Mark where platelets are.
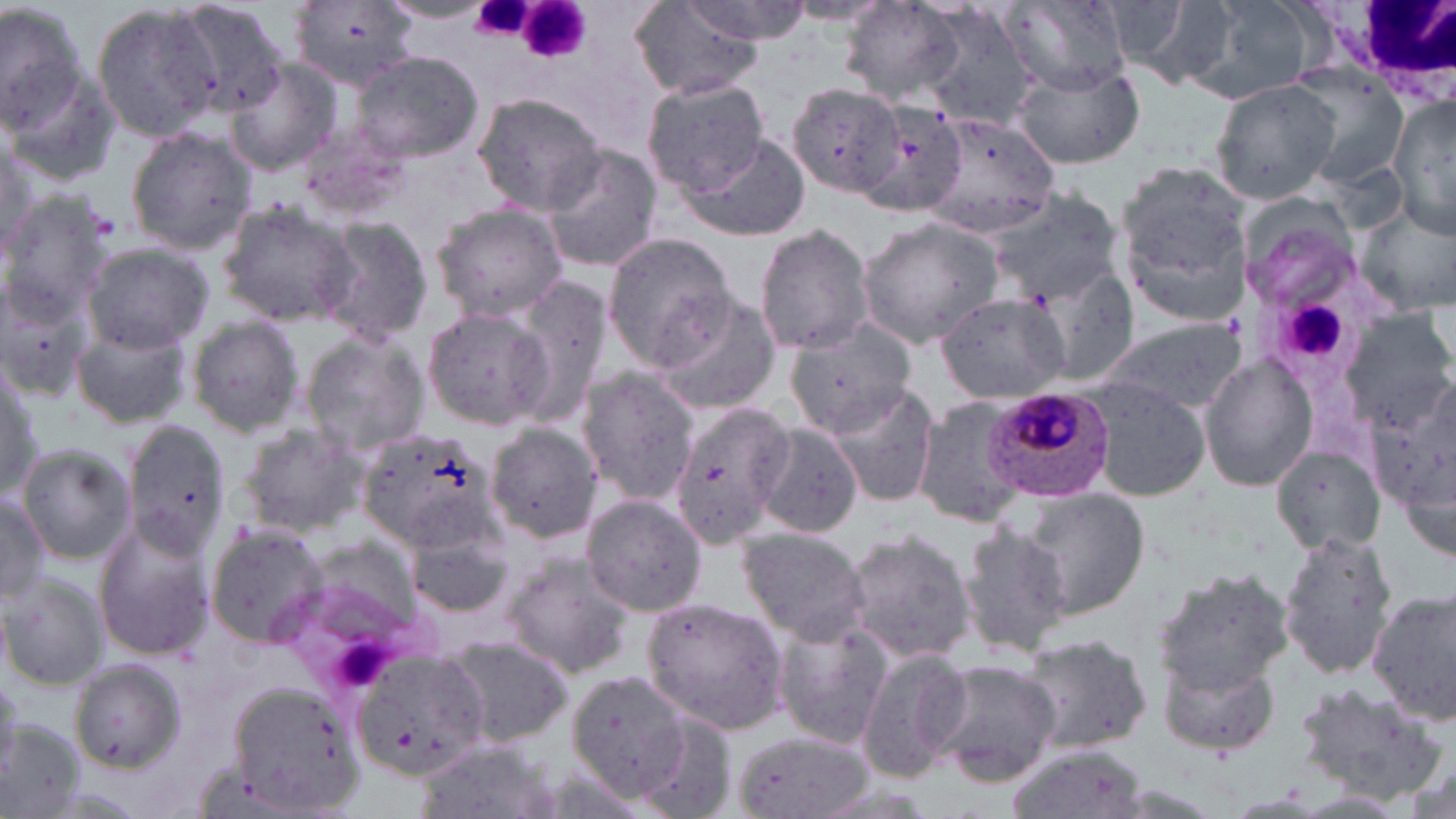
Approximate bounding boxes as (x1, y1, x2, y2) in pixels.
Platelets: (465, 0, 541, 42), (508, 0, 594, 63), (1281, 299, 1343, 360).

Summary:
  - White blood cell locations: (1328, 0, 1456, 98)
  - Uninfected red blood cell locations: (0, 0, 95, 153), (290, 0, 424, 93), (690, 0, 812, 43), (378, 1, 489, 23), (999, 1, 1128, 92), (1117, 1, 1239, 91), (1195, 1, 1322, 106), (788, 2, 890, 26), (839, 2, 968, 104), (168, 4, 297, 111), (629, 5, 764, 98), (906, 5, 1043, 132), (95, 6, 223, 140), (350, 52, 483, 162), (225, 57, 344, 176), (1013, 65, 1143, 169), (1293, 71, 1409, 188), (641, 77, 770, 195), (1210, 79, 1342, 205), (791, 84, 903, 198), (470, 94, 605, 211), (1387, 96, 1455, 238), (863, 102, 970, 215), (922, 113, 1062, 235), (296, 124, 409, 220), (124, 126, 257, 253), (680, 134, 811, 242), (0, 136, 44, 262), (539, 143, 663, 273), (1115, 167, 1253, 322), (983, 188, 1125, 304), (1234, 191, 1360, 310), (0, 192, 114, 322), (1352, 197, 1456, 312), (217, 204, 357, 325), (430, 204, 568, 321), (315, 218, 434, 342), (857, 219, 1003, 349), (754, 224, 877, 355), (604, 233, 737, 365), (81, 242, 214, 352), (1036, 263, 1140, 387), (0, 271, 101, 404), (509, 278, 613, 425), (654, 291, 781, 415), (937, 294, 1070, 404), (1338, 306, 1455, 426), (423, 309, 553, 429), (185, 314, 305, 437), (1098, 317, 1246, 415), (787, 321, 916, 437), (70, 325, 193, 427), (302, 333, 431, 456), (1199, 353, 1318, 492), (1358, 363, 1455, 522), (1, 365, 44, 500), (575, 369, 699, 503), (1085, 379, 1212, 500), (826, 384, 941, 511), (909, 398, 1030, 527), (668, 402, 798, 547), (120, 420, 233, 563), (757, 422, 864, 539), (238, 423, 371, 535), (355, 426, 494, 550), (483, 426, 606, 543), (1273, 443, 1391, 554), (19, 444, 136, 563), (0, 488, 50, 606), (1020, 488, 1149, 619), (581, 495, 706, 616), (92, 517, 219, 662), (957, 521, 1071, 660), (205, 525, 332, 646), (736, 528, 874, 645), (403, 529, 516, 618), (840, 529, 974, 665), (1277, 532, 1396, 681), (315, 542, 419, 632), (502, 554, 637, 678), (1149, 567, 1295, 694), (1, 574, 109, 690), (1369, 588, 1454, 723), (644, 596, 789, 734), (772, 621, 891, 749), (1012, 631, 1154, 757), (442, 635, 576, 748), (856, 646, 972, 782), (354, 648, 495, 782), (1159, 655, 1285, 756), (71, 660, 186, 771), (930, 661, 1061, 786), (569, 669, 692, 796), (223, 676, 370, 812), (1293, 682, 1449, 801), (633, 715, 739, 819), (0, 719, 87, 819), (730, 731, 871, 819), (414, 740, 562, 819), (1003, 745, 1151, 819)
  - Plasmodium malariae-infected red blood cell locations: (982, 384, 1116, 501)
  - Slide-level diagnosis: Plasmodium malariae
  - Magnification: 1000x
  - Preparation: thin blood film
  - Stain: May-Grünwald-Giemsa
  - Image size: 1456×819 pixels
  - Modality: light microscopy
  - Field of view: single